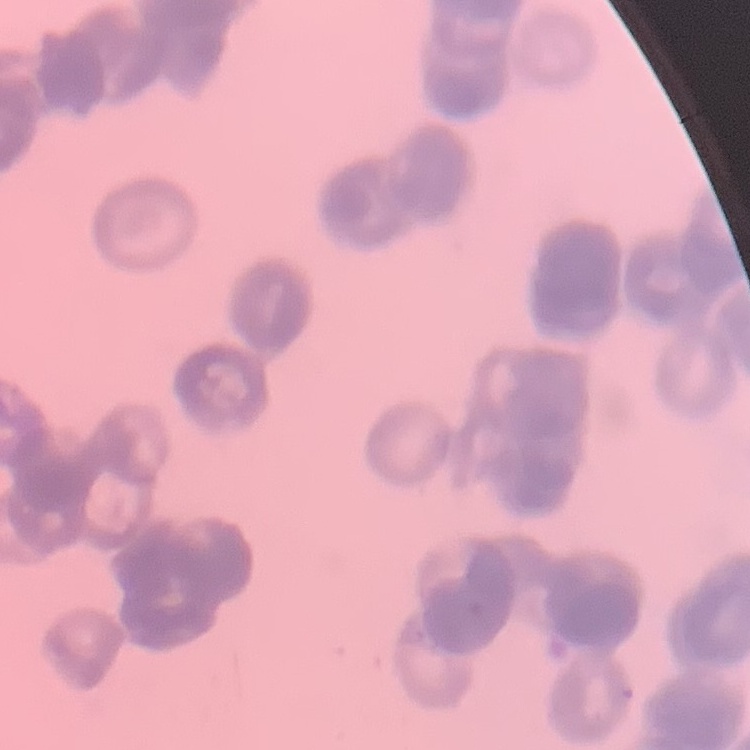 The erythrocytes show rouleaux formation. Field's or Giemsa stain. Square crop of a larger photomicrograph. Thin blood film.